Outline each blood parasite and name the species.
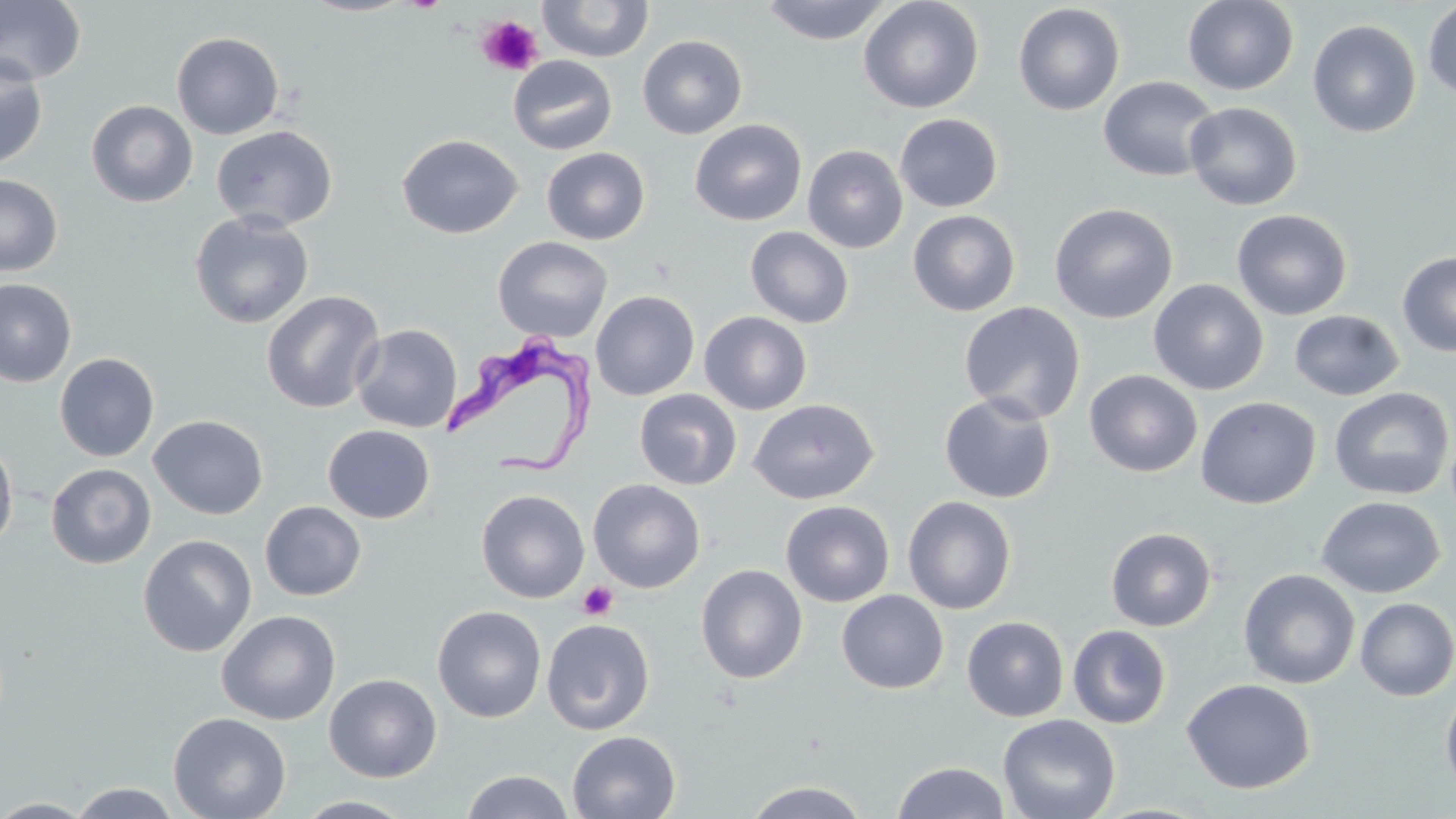

Approximate bounding boxes as (x1,y1)-(x2,y2) corner pairs in pixels.
Trypanosoma brucei: (441,332)-(598,476).
No Plasmodium falciparum, Plasmodium ovale, Plasmodium malariae, Plasmodium vivax, or Babesia divergens observed.

Uninfected red blood cell locations: (0,0)-(86,85), (298,0)-(415,17), (537,0)-(653,62), (760,0)-(893,45), (858,0)-(984,114), (1182,0)-(1300,96), (1422,1)-(1456,100), (1013,3)-(1125,115), (1307,19)-(1421,138), (172,31)-(284,140), (637,35)-(747,139), (0,54)-(49,170), (507,55)-(617,155), (1098,76)-(1221,182), (86,99)-(198,207), (1185,101)-(1302,211), (895,113)-(1003,212), (690,119)-(807,226), (211,125)-(337,231), (397,134)-(523,238), (803,145)-(907,253), (542,147)-(650,245), (0,174)-(62,277), (1049,203)-(1177,323), (1231,208)-(1353,321), (907,209)-(1020,316), (189,210)-(315,329), (745,226)-(853,328), (493,236)-(613,343), (1397,252)-(1456,357), (0,278)-(77,387), (1148,279)-(1268,395), (590,290)-(699,400), (261,291)-(384,414), (959,301)-(1085,424), (1289,309)-(1404,401), (699,311)-(812,414), (352,323)-(462,433), (54,353)-(159,461), (1084,369)-(1203,477), (1329,387)-(1454,501), (634,389)-(742,490), (939,393)-(1056,504), (1195,396)-(1321,509), (748,398)-(879,505), (148,415)-(268,520), (323,425)-(434,523), (0,436)-(19,554), (46,464)-(156,569), (588,479)-(705,593), (476,490)-(589,603), (903,496)-(1016,615), (1316,496)-(1445,599), (781,500)-(895,607), (260,501)-(366,601), (1105,526)-(1216,631), (137,534)-(256,657), (696,564)-(808,683), (1238,569)-(1360,689), (836,590)-(948,694), (1355,597)-(1456,701), (432,605)-(546,723), (217,610)-(341,725), (962,615)-(1069,722), (542,618)-(654,735), (1067,625)-(1171,729), (324,673)-(442,782), (1181,678)-(1316,795), (1440,684)-(1456,803), (168,712)-(291,819), (998,713)-(1120,819), (567,731)-(681,819), (892,761)-(1010,819), (460,770)-(575,818), (744,780)-(869,818), (68,782)-(183,819), (294,796)-(418,818), (0,798)-(97,818). Platelet locations: (477,15)-(543,76), (577,581)-(618,621). Slide-level diagnosis: Trypanosoma brucei. Light microscopy. Thin blood smear. 1000x magnification. May-Grünwald-Giemsa-stained preparation. One field of a larger specimen. Image is 1456×819 pixels.